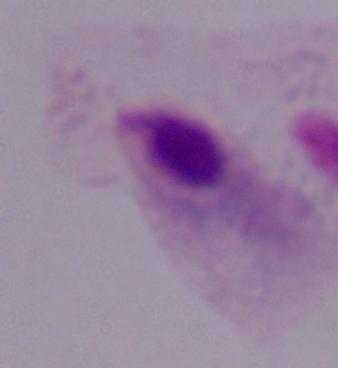
modality = micrograph
identification = trichomonad
magnification = 1000x